Point out each malaria parasite.
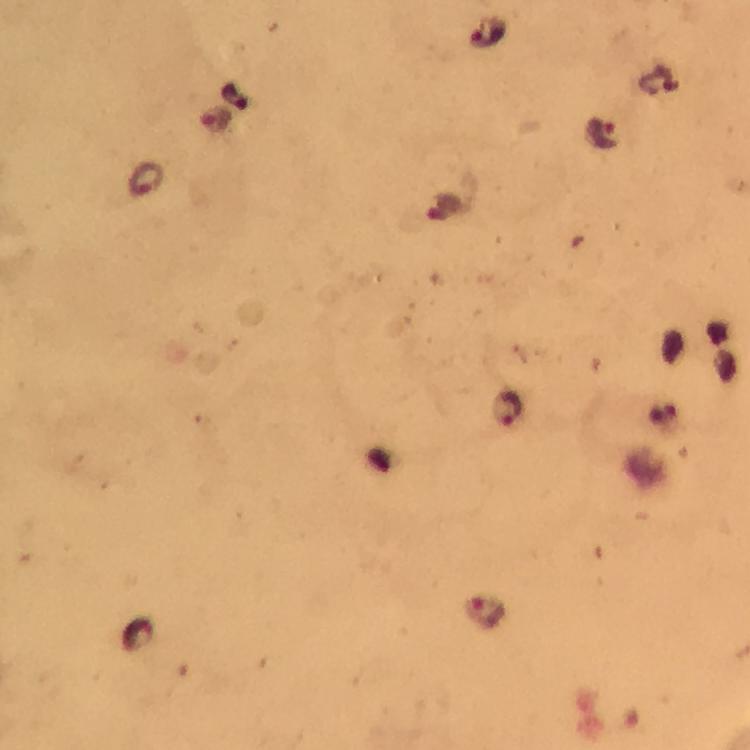
Approximate centers as {x, y} in pixels.
Malaria parasites: {489, 33}, {215, 120}, {602, 136}, {146, 180}, {444, 209}, {507, 411}, {486, 614}.

image size = 750×750 pixels
preparation = thick smear
stain = Giemsa
capture = smartphone mounted on the microscope
context = from a malaria diagnostic workup
cropped from = one field of view
magnification = 100x
immersion oil = used